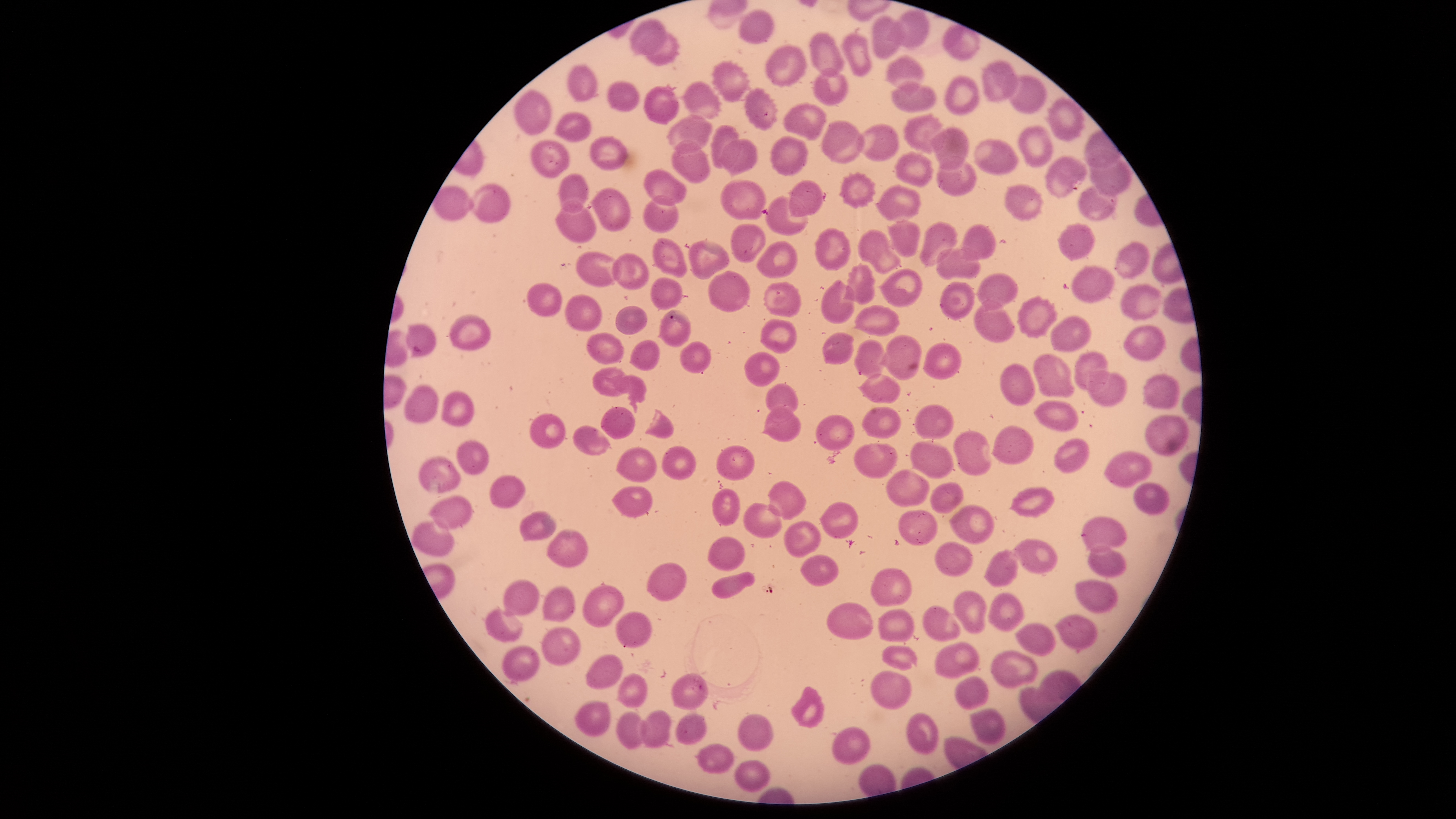 Approximate bounding boxes as [left, top, right, bottom] in pixels. Uninfected red blood cells: [740, 10, 774, 43], [897, 10, 929, 48], [873, 16, 905, 58], [628, 20, 667, 55], [944, 24, 979, 60], [809, 33, 844, 74], [644, 34, 679, 66], [843, 34, 872, 78], [765, 46, 806, 86], [886, 55, 924, 97], [711, 60, 750, 101], [982, 61, 1017, 100], [568, 65, 599, 100], [815, 69, 848, 105], [946, 75, 979, 114], [1009, 75, 1046, 113], [609, 82, 639, 110], [682, 82, 722, 119], [891, 82, 936, 111], [645, 85, 679, 124], [745, 88, 778, 131], [514, 90, 551, 135], [1044, 98, 1085, 142], [784, 102, 827, 141], [555, 113, 591, 142], [904, 113, 944, 153], [667, 114, 712, 155], [821, 121, 866, 163], [856, 124, 899, 162], [711, 125, 739, 169], [931, 126, 967, 171], [1020, 127, 1053, 167], [771, 136, 809, 175], [590, 137, 629, 171], [718, 138, 757, 178], [530, 140, 570, 177], [672, 140, 711, 183], [972, 140, 1019, 174], [895, 153, 933, 187], [937, 157, 976, 195], [1047, 157, 1087, 197], [643, 170, 687, 205], [839, 173, 875, 208], [560, 174, 587, 213], [721, 180, 765, 219], [789, 180, 823, 217], [466, 184, 510, 222], [876, 184, 922, 220], [1006, 185, 1042, 221], [1078, 186, 1117, 221], [591, 189, 632, 230], [644, 196, 678, 232], [766, 196, 808, 236], [554, 199, 596, 242], [887, 220, 920, 257], [920, 222, 957, 264], [732, 224, 764, 261], [1059, 224, 1094, 261], [961, 225, 995, 262], [814, 227, 850, 271], [858, 230, 903, 272], [653, 238, 686, 277], [689, 240, 730, 280], [756, 240, 799, 278], [1113, 240, 1150, 278], [936, 248, 981, 279], [577, 251, 617, 285], [612, 252, 650, 288], [844, 263, 875, 304], [878, 268, 922, 307], [1072, 268, 1115, 303], [708, 271, 749, 311], [977, 273, 1019, 312], [649, 276, 683, 309], [822, 280, 855, 324], [763, 282, 802, 317], [940, 282, 973, 320], [527, 283, 562, 316], [1121, 285, 1161, 320], [566, 295, 602, 331], [1017, 295, 1057, 337], [974, 298, 1014, 342], [853, 305, 902, 335], [615, 306, 648, 333], [658, 309, 690, 346], [448, 315, 490, 349], [1051, 316, 1091, 351], [761, 320, 796, 353], [405, 325, 436, 357], [1123, 325, 1165, 360], [823, 332, 855, 364], [586, 333, 624, 365], [882, 336, 921, 378], [629, 339, 660, 371], [854, 339, 887, 377], [680, 341, 711, 373], [922, 343, 961, 380], [745, 350, 781, 386], [1074, 352, 1108, 389], [1034, 354, 1074, 397], [1000, 364, 1035, 404], [592, 367, 629, 396], [1089, 370, 1128, 407], [858, 373, 903, 402], [1144, 374, 1179, 408], [766, 383, 799, 411], [405, 386, 437, 422], [442, 391, 473, 426], [1034, 401, 1078, 431], [914, 405, 955, 438], [761, 406, 801, 443], [601, 407, 635, 440], [862, 407, 901, 438], [530, 412, 565, 448], [815, 415, 854, 450], [1144, 416, 1189, 456], [573, 426, 609, 455], [992, 427, 1035, 463], [954, 431, 989, 476], [1053, 437, 1090, 474], [458, 440, 489, 474], [911, 440, 953, 479], [853, 442, 898, 479], [717, 446, 755, 480], [662, 447, 695, 478], [616, 448, 656, 482], [1104, 452, 1151, 487], [419, 457, 461, 494], [885, 469, 930, 505], [490, 476, 526, 508], [768, 480, 807, 520], [929, 482, 964, 512], [1135, 483, 1171, 515], [612, 486, 652, 515], [1009, 487, 1057, 516], [712, 488, 740, 525], [428, 496, 473, 528], [819, 502, 859, 538], [744, 503, 782, 538], [949, 505, 995, 544], [520, 510, 556, 541], [897, 510, 937, 545], [1082, 517, 1128, 550], [784, 520, 820, 557], [411, 521, 455, 556], [546, 530, 588, 567], [708, 537, 746, 571], [1009, 539, 1057, 572], [935, 542, 974, 576], [1089, 546, 1127, 577], [983, 550, 1018, 585], [800, 555, 839, 586], [646, 563, 687, 600], [871, 566, 912, 606], [711, 571, 756, 598], [501, 580, 540, 616], [1075, 580, 1118, 613], [584, 585, 624, 626], [542, 587, 574, 621], [953, 591, 987, 634], [988, 593, 1024, 632], [827, 603, 873, 639], [922, 606, 960, 641], [485, 608, 523, 642], [878, 609, 915, 642], [616, 612, 652, 646], [1055, 616, 1097, 649], [1016, 623, 1056, 656], [543, 627, 580, 666], [934, 642, 978, 680], [501, 645, 539, 682], [882, 645, 917, 669], [991, 650, 1038, 687], [585, 655, 623, 690], [872, 671, 912, 710], [615, 673, 649, 707], [671, 674, 709, 709], [956, 676, 990, 709], [791, 687, 824, 728], [575, 702, 610, 737], [616, 712, 644, 750], [637, 712, 671, 748], [676, 714, 706, 743], [738, 715, 772, 751], [831, 728, 870, 764], [695, 744, 733, 772], [735, 760, 769, 793]. Thin blood smear. Single field of view. Photographed with a smartphone camera through the microscope eyepiece. Image is 1456×819 pixels. Giemsa-stained preparation. Circular visible region. Presence: no malaria parasites identified.